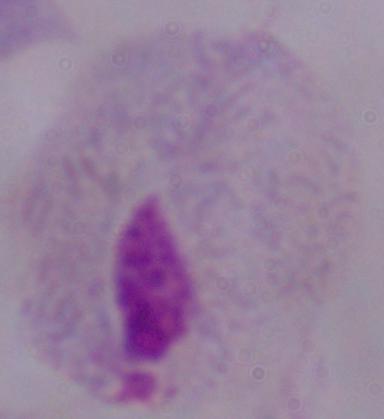

magnification = 1000x
identification = trichomonad
modality = micrograph